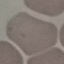
result = no malaria parasites detected
preparation = thin blood smear
capture = smartphone camera at the microscope eyepiece
stain = Giemsa
image type = automatically extracted cell patch, resized to 64 × 64 pixels